State the blood parasite species.
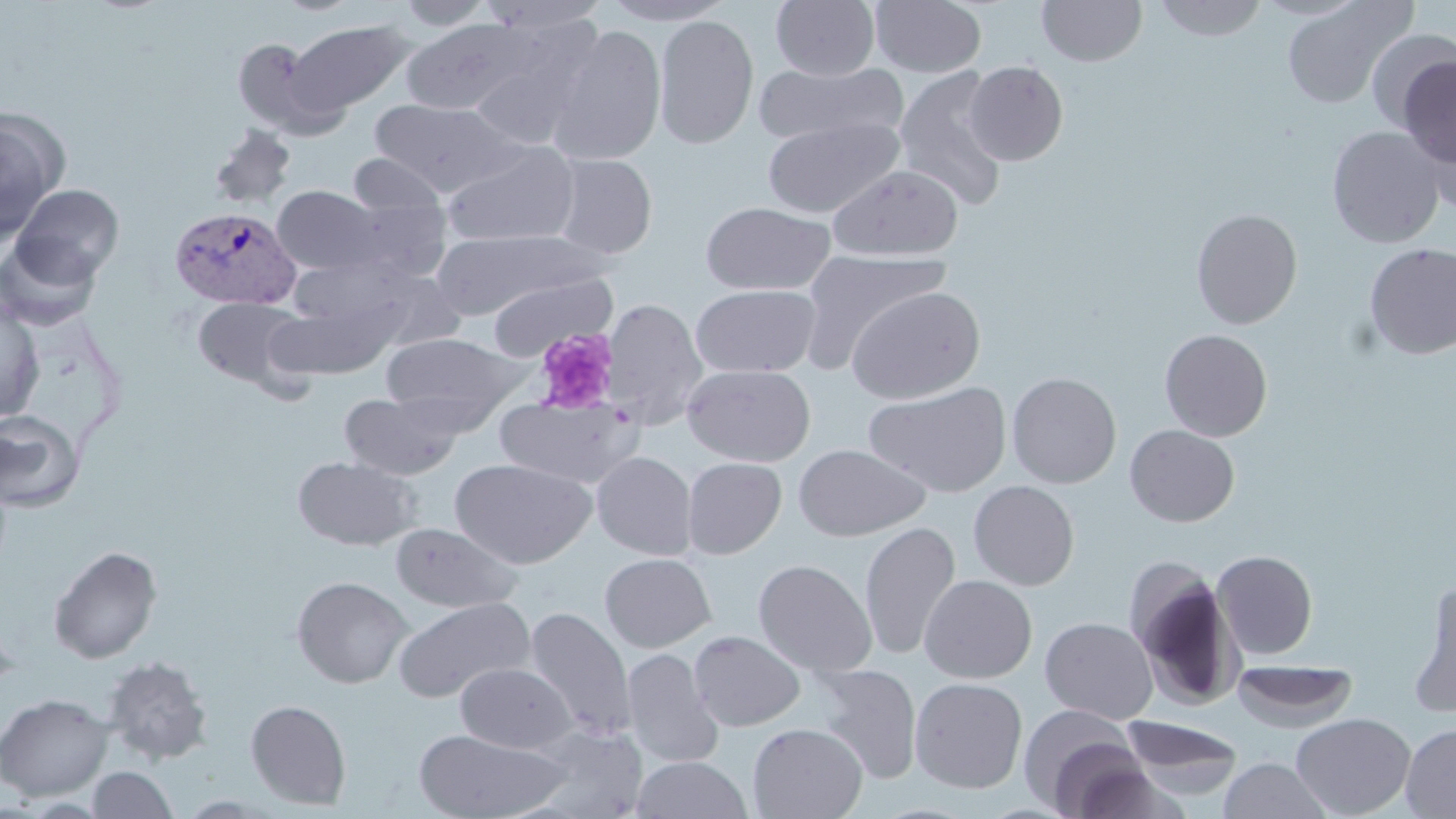

Plasmodium vivax.

Summary:
  - Coordinate format: approximate bounding boxes as (x1, y1, x2, y2) in pixels
  - Platelet locations: (534, 327, 618, 415)
  - Plasmodium vivax-infected red blood cell locations: (169, 205, 302, 309)
  - Uninfected red blood cell locations: (273, 0, 365, 15), (394, 0, 496, 29), (477, 0, 610, 34), (600, 0, 737, 25), (870, 0, 986, 77), (1036, 0, 1148, 67), (1152, 0, 1270, 41), (1281, 0, 1417, 110), (771, 1, 879, 80), (653, 14, 759, 149), (400, 17, 543, 115), (460, 17, 604, 148), (285, 19, 418, 117), (546, 25, 667, 166), (1367, 29, 1455, 135), (232, 36, 337, 136), (1396, 54, 1456, 173), (754, 60, 909, 148), (964, 60, 1069, 165), (893, 66, 1010, 211), (369, 98, 526, 195), (0, 111, 68, 239), (762, 116, 904, 218), (209, 123, 297, 209), (1326, 125, 1446, 249), (440, 141, 581, 248), (348, 153, 447, 219), (550, 153, 658, 259), (827, 164, 963, 261), (11, 183, 124, 284), (272, 185, 384, 275), (700, 201, 836, 296), (1190, 208, 1303, 329), (431, 229, 607, 319), (0, 238, 101, 331), (1363, 242, 1456, 359), (796, 251, 949, 370), (486, 271, 616, 361), (690, 283, 821, 378), (846, 285, 986, 404), (192, 296, 310, 390), (0, 298, 45, 423), (601, 298, 708, 431), (1159, 328, 1273, 442), (380, 331, 527, 420), (681, 363, 815, 467), (1006, 371, 1122, 488), (865, 380, 1012, 498), (339, 391, 463, 480), (494, 395, 643, 489), (0, 409, 85, 513), (1124, 424, 1239, 527), (793, 444, 929, 541), (591, 451, 697, 560), (292, 455, 420, 550), (452, 457, 596, 568), (682, 457, 786, 559), (968, 480, 1079, 591), (860, 520, 961, 661), (389, 522, 522, 613), (48, 545, 162, 664), (1212, 550, 1317, 659), (600, 552, 716, 653), (1125, 558, 1245, 712), (753, 559, 877, 677), (919, 574, 1037, 684), (292, 575, 412, 688), (1407, 579, 1456, 717), (392, 596, 535, 703), (523, 606, 636, 741), (0, 609, 22, 698), (1040, 617, 1158, 724), (689, 630, 805, 732), (623, 649, 724, 771), (102, 655, 213, 764), (1232, 660, 1358, 732), (455, 662, 576, 753), (809, 663, 923, 783), (909, 677, 1028, 793), (0, 693, 114, 801), (245, 699, 352, 810), (1022, 708, 1154, 815), (1290, 712, 1416, 818), (1119, 715, 1245, 800), (747, 723, 867, 819), (1400, 723, 1456, 818), (413, 728, 570, 819), (631, 755, 753, 818), (1217, 757, 1334, 818), (87, 766, 179, 819)
  - Preparation: thin blood film
  - Field of view: single
  - Stain: May-Grünwald-Giemsa
  - Modality: light microscopy
  - Image size: 1456×819 pixels
  - Magnification: 1000x